State which cell type is depicted.
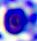
This is a leukocyte.

Photomicrograph. Captured at 400x magnification.